State the preparation type.
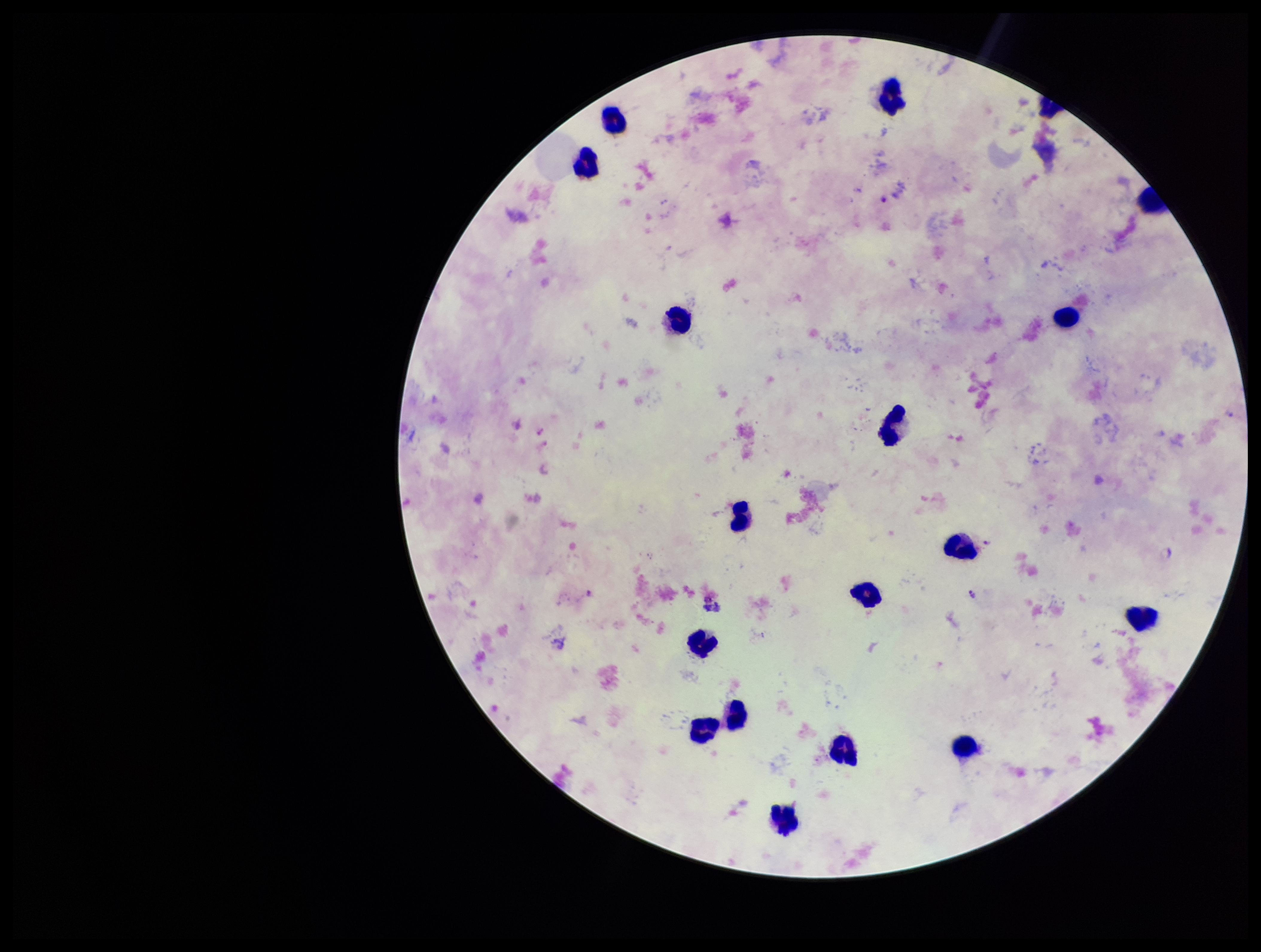

A thick smear.

stain = Giemsa
capture = smartphone photograph through the microscope eyepiece
patient malaria status = infected
image size = 1261×952 pixels
field of view = one from this slide
leukocyte count = 18
parasite count = 3
Plasmodium parasites = detected
species reported for this patient = Plasmodium falciparum